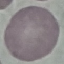

malaria status = uninfected
capture = smartphone camera at the microscope eyepiece
stain = Giemsa
image type = automatically extracted cell patch, resized to 64 × 64 pixels
preparation = thin blood smear